Give the preparation type.
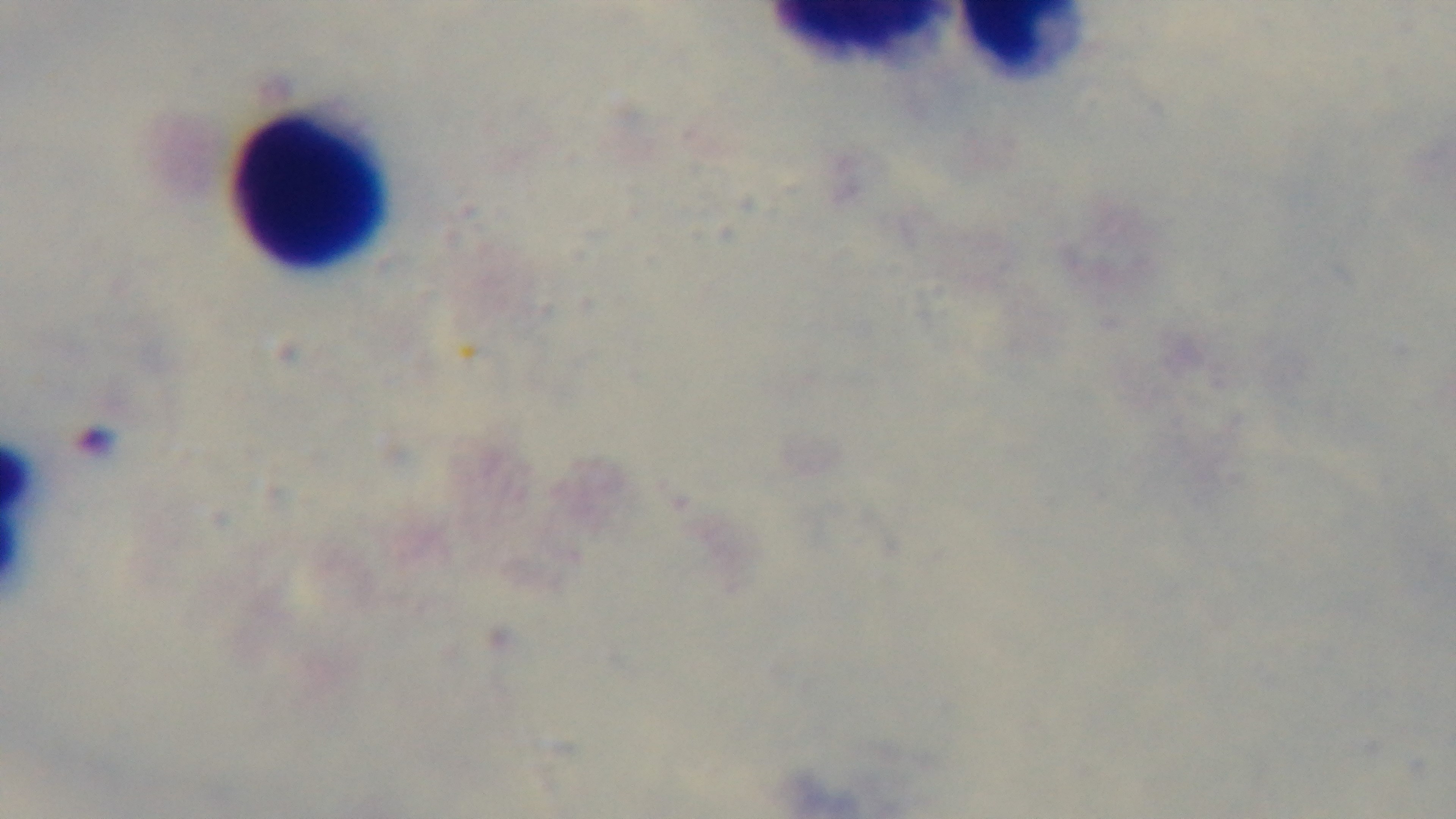
Thick.

Giemsa stain. Malaria status: negative. 100x oil-immersion objective. One field from the slide. Mounted 4K digital camera. Photomicrograph.